Identify the parasite.
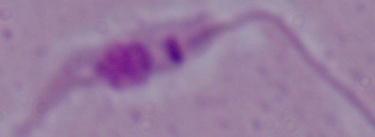
Leishmania.

1000x magnification. Photomicrograph.